Describe the morphology of the red blood cells.
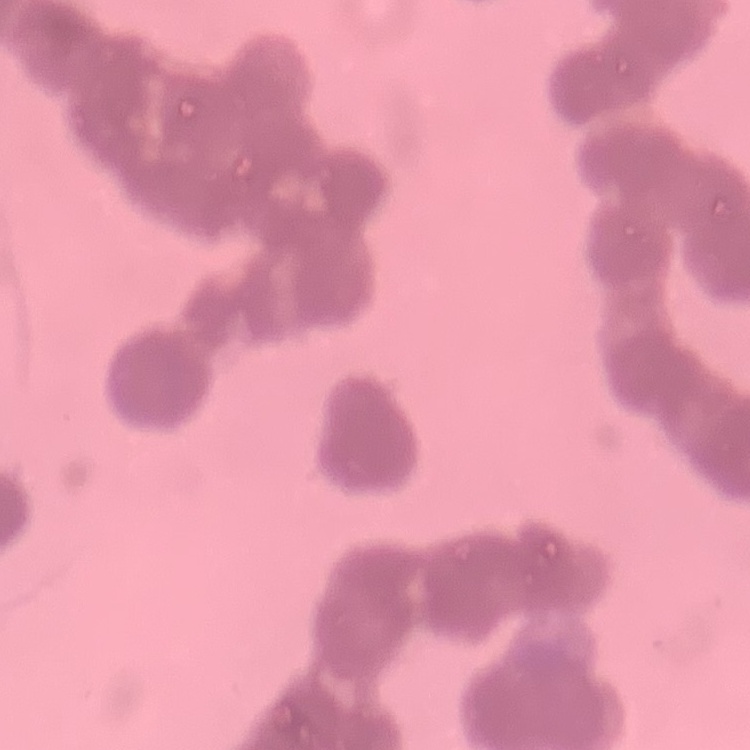

Rouleaux formation.

Summary:
  - Preparation: thin blood film
  - Image type: one tile cut from a larger photomicrograph
  - Stain: Field's or Giemsa